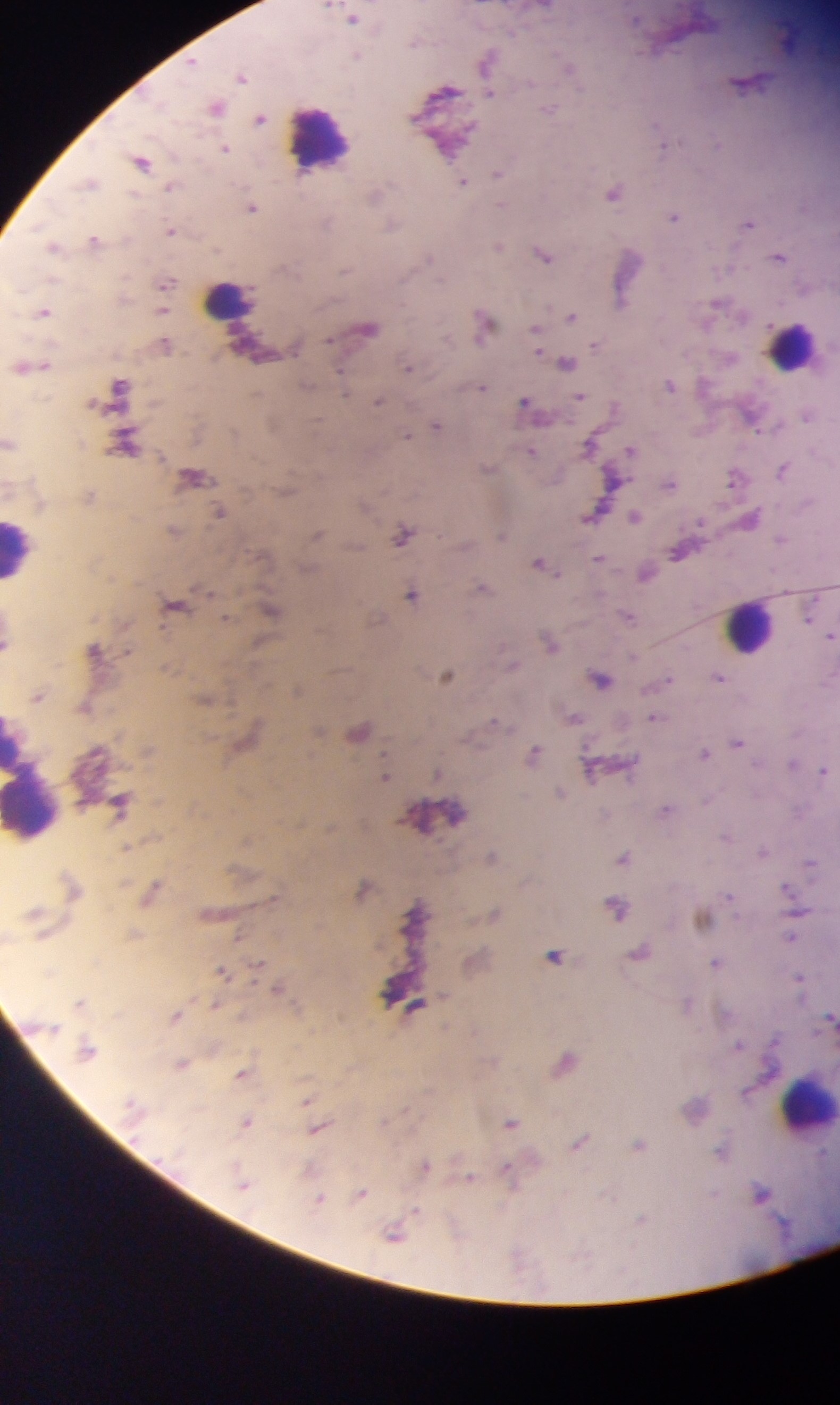
Plasmodium parasite locations = approximate centers as (x, y) in pixels: (544, 7), (352, 19), (415, 41), (357, 55), (487, 61), (192, 63), (567, 67), (241, 76), (746, 82), (444, 92), (490, 93), (215, 107), (549, 110), (259, 119), (663, 145), (224, 148), (141, 161), (497, 174), (462, 182), (89, 183), (170, 188), (613, 193), (376, 194), (500, 204), (251, 208), (674, 217), (326, 221), (747, 223), (391, 227), (170, 230), (94, 240), (498, 246), (52, 247), (542, 254), (428, 257), (779, 257), (345, 270), (165, 283), (622, 299), (42, 312), (162, 312), (570, 317), (483, 324), (368, 328), (535, 332), (596, 345), (165, 346), (565, 363), (33, 367), (408, 367), (670, 384), (306, 385), (119, 387), (342, 387), (481, 387), (580, 396), (377, 402), (525, 404), (612, 408), (806, 416), (435, 425), (406, 435), (8, 443), (125, 443), (589, 446), (631, 450), (531, 451), (487, 469), (782, 470), (193, 478), (614, 479), (733, 479), (670, 484), (218, 512), (594, 512), (634, 516), (750, 518), (173, 532), (316, 535), (402, 535), (500, 535), (781, 539), (677, 551), (599, 558), (540, 564), (645, 573), (481, 587), (411, 595), (175, 604), (270, 610), (810, 613), (627, 616), (831, 635), (549, 642), (5, 644), (94, 650), (511, 664), (446, 675), (718, 677), (599, 678), (666, 680), (296, 690), (36, 696), (203, 700), (85, 707), (572, 717), (655, 717), (494, 721), (358, 731), (737, 742), (704, 753), (533, 754), (791, 764), (590, 770), (823, 770), (437, 775), (384, 776), (559, 793), (119, 802), (665, 810), (726, 836), (762, 851), (491, 857), (623, 857), (810, 864), (786, 887), (362, 888), (151, 889), (616, 907), (494, 914), (702, 919), (790, 937), (640, 952), (554, 956), (716, 962), (220, 971), (797, 977), (277, 987), (78, 1003), (686, 1004), (414, 1007), (174, 1015), (829, 1016), (738, 1045), (86, 1049), (565, 1061), (181, 1063), (241, 1075), (306, 1099), (246, 1122), (510, 1122), (317, 1129), (579, 1142), (638, 1146), (720, 1152), (424, 1165), (508, 1172), (470, 1178), (241, 1181), (761, 1193), (360, 1194), (318, 1201), (395, 1233)
field of view = single
preparation = thick blood film
leukocyte locations = approximate centers as (x, y) in pixels: (318, 139), (229, 297), (791, 346), (19, 549), (750, 627), (31, 788), (806, 1104)
image size = 840×1405 pixels
capture = mobile-phone photograph through a microscope
country = Ghana